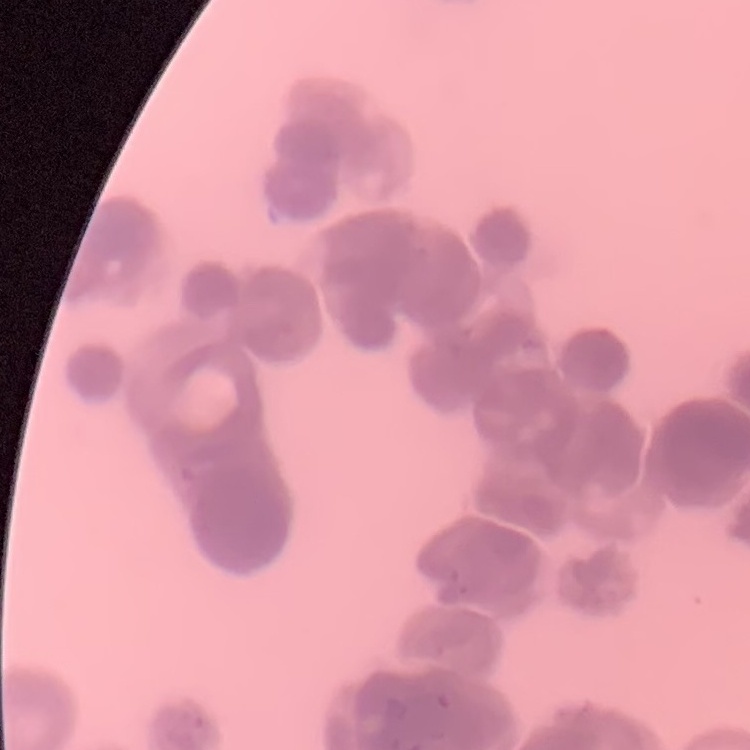

erythrocyte morphology = rouleaux formation
preparation = thin blood smear
image type = square crop of a larger photomicrograph
stain = Field's or Giemsa